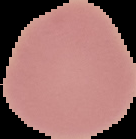
Summary:
  - Preparation: thin blood smear
  - Image type: segmented cell region on a black background
  - Malaria status: uninfected
  - Image size: 136×139 pixels